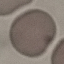
malaria status = uninfected
stain = Giemsa
preparation = thin blood smear
capture = smartphone through the microscope eyepiece
image type = automatically extracted cell patch, resized to 64 × 64 pixels